Classify this cell by malaria status.
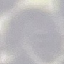
It is uninfected.

Cell patch, automatically extracted from a larger field of view and resized to 64 × 64 pixels. Giemsa stain. Thin blood smear. Photographed with a smartphone camera at the microscope eyepiece.